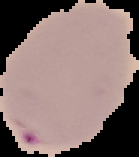
Image is 139×157 pixels. The area outside the segmented cell region is set to black. Result: Plasmodium parasites identified. From a thin blood smear.